Classify this cell by malaria status.
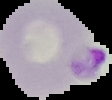
It is parasitized.

Image is 112×100 pixels. From a thin blood film. Cell region segmented out of the field of view; the surrounding area is masked to black.